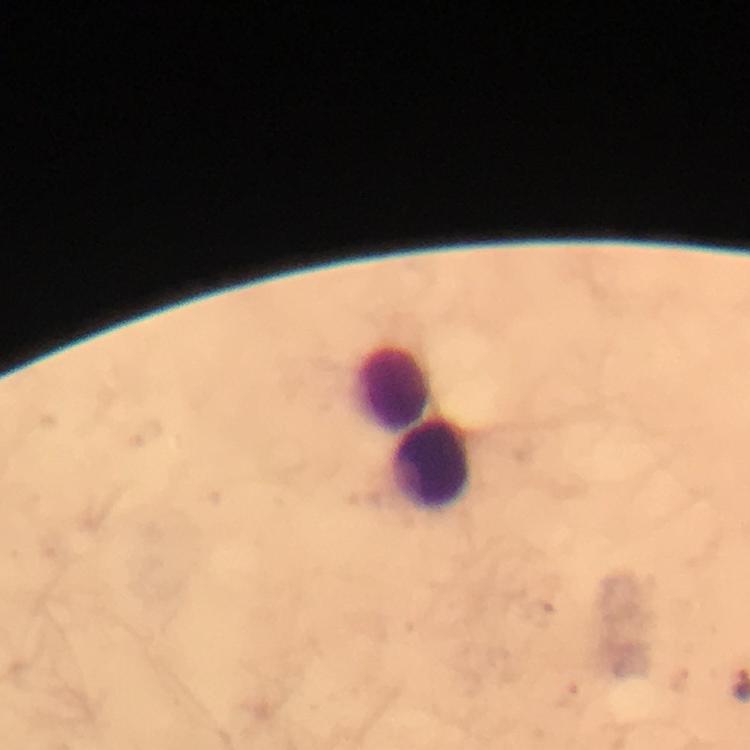 Approximate object centers, in pixels from the top-left corner. Leukocyte locations: (x=394, y=390), (x=433, y=467). Photographed through the microscope with a smartphone camera. From a diagnostic examination for malaria. Image is 750×750 pixels. Immersion oil applied. Malaria parasites: none seen. At 100x magnification. A crop from one field of view. Giemsa-stained preparation. Thick smear.